Report the malaria status.
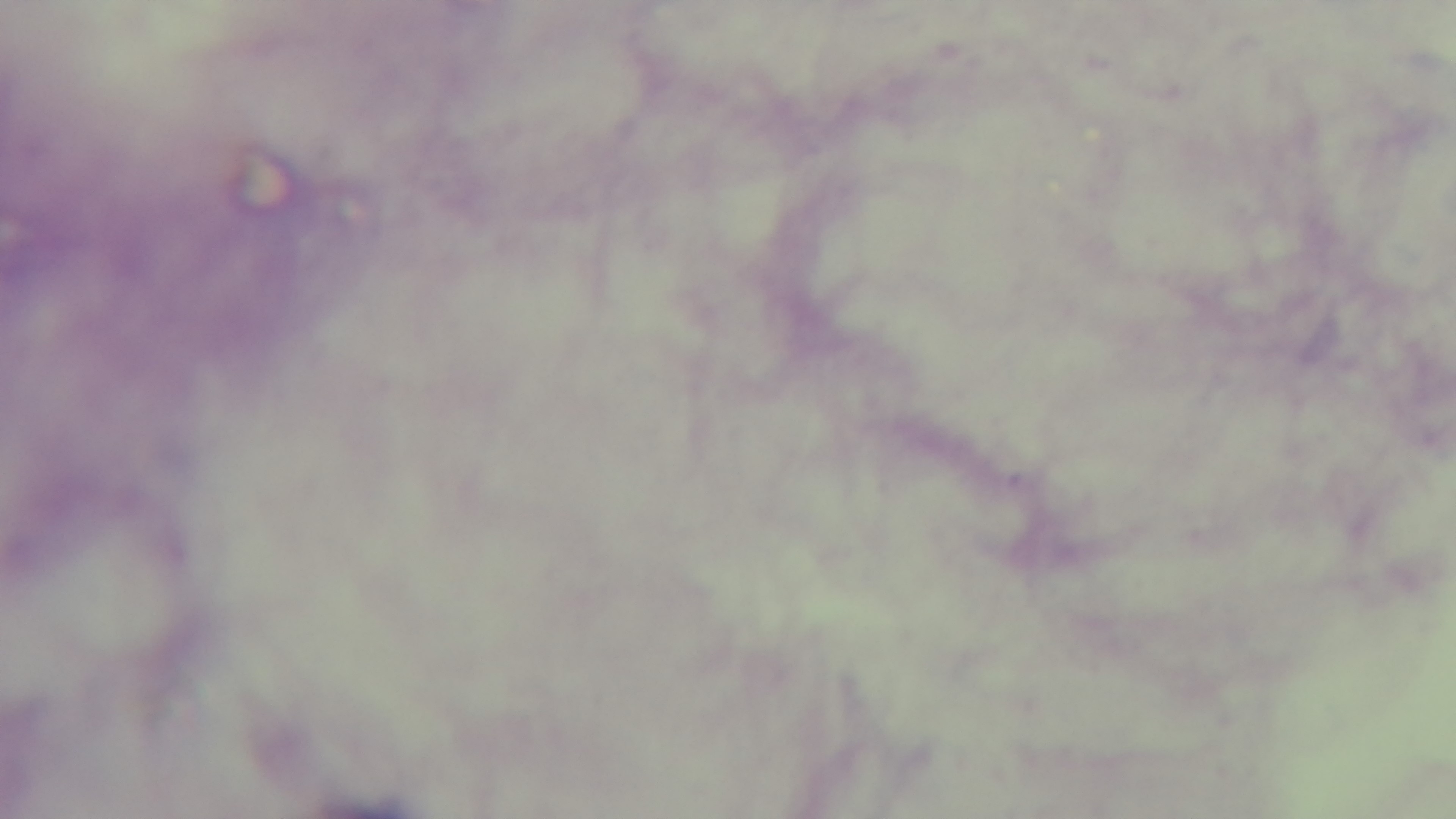

Negative.

Light microscopy. 100x oil-immersion objective. Giemsa stain. Single field of view. Preparation: thick blood film. Captured with a mounted 4K digital camera.